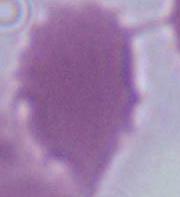

Captured at 1000x magnification. Micrograph. A red blood cell is shown.